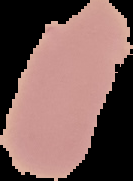
Cell region segmented out of the field of view; the surrounding area is masked to black. From a thin blood smear. Image is 133×181 pixels. Result: negative for malaria parasites.